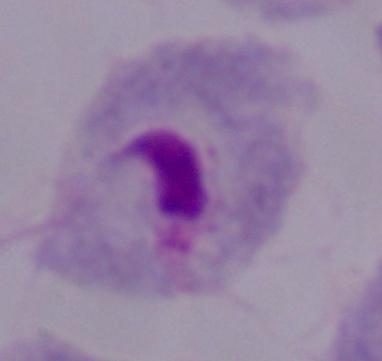

Summary:
  - Magnification: 1000x
  - Identification: trichomonad
  - Modality: micrograph